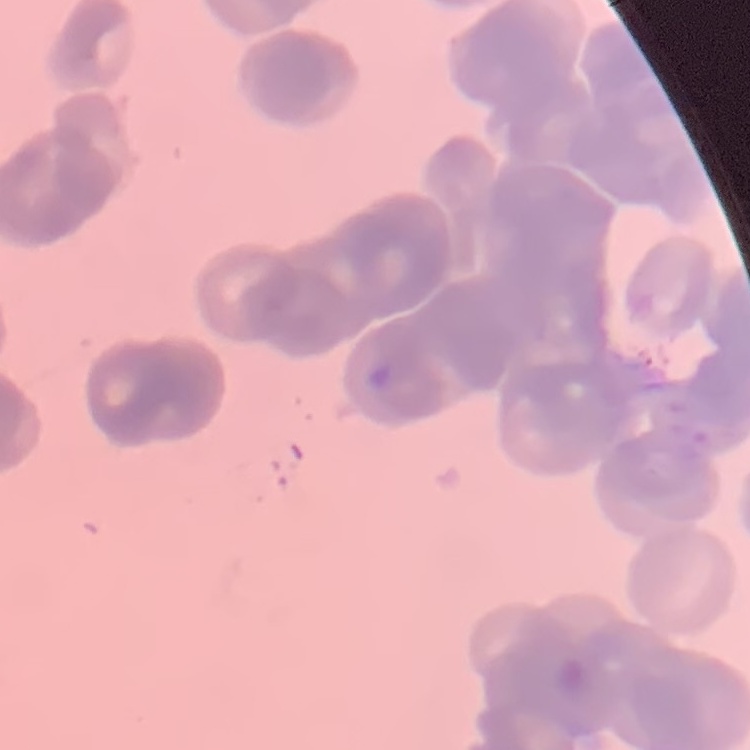
The erythrocytes exhibit rouleaux formation. Thin blood smear. Field's or Giemsa stain. Square crop of a larger photomicrograph.